Name the cell type shown.
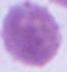
An erythrocyte.

Micrograph. Captured at 1000x magnification.